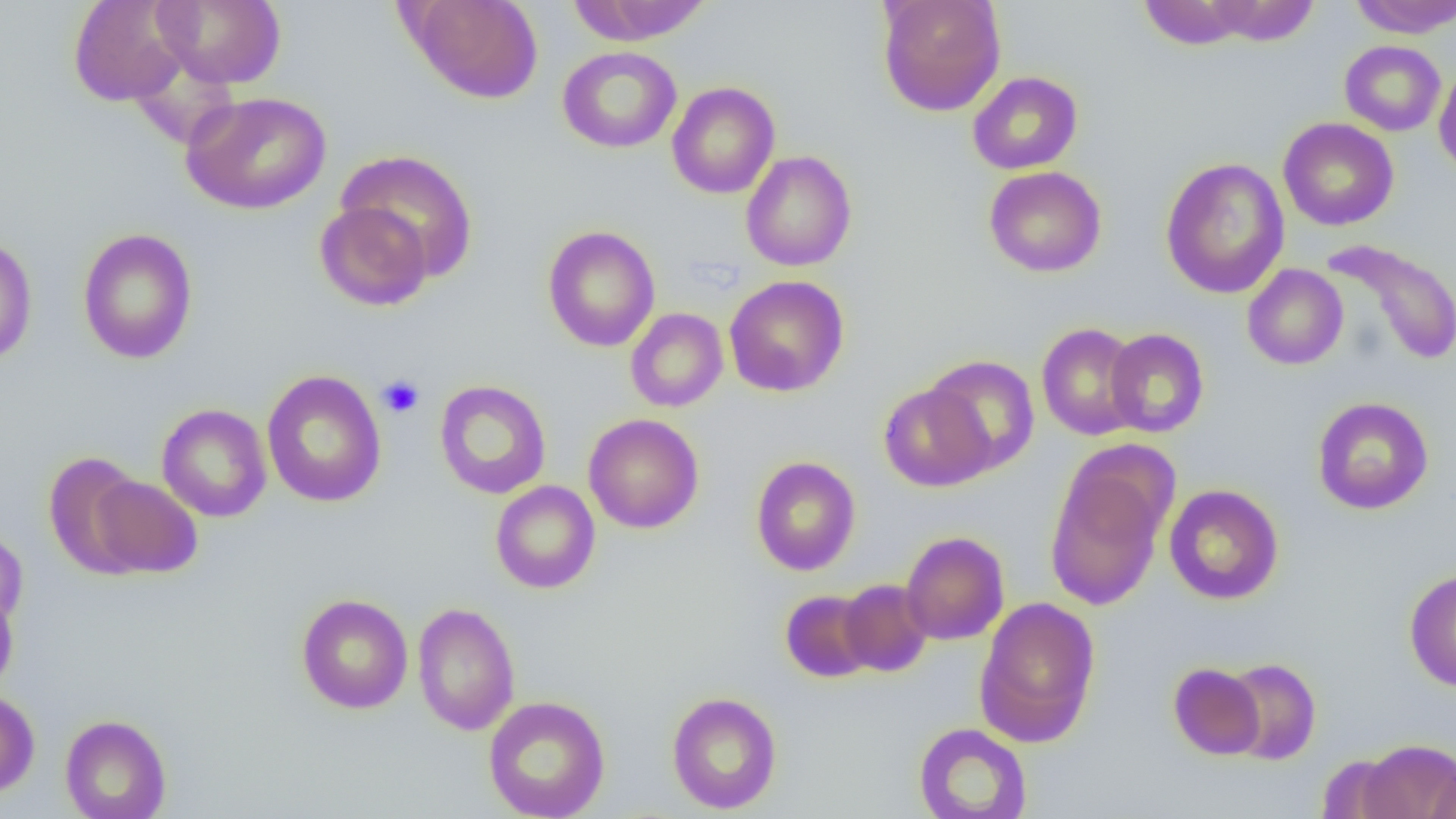
Summary:
  - Coordinate format: approximate bounding boxes as [x1, y1, x2, y2] in pixels
  - Uninfected red blood cell locations: [68, 0, 191, 107], [152, 0, 286, 89], [406, 0, 542, 104], [876, 0, 1007, 116], [1347, 0, 1456, 38], [567, 1, 714, 45], [1138, 1, 1255, 50], [1203, 1, 1320, 46], [1339, 40, 1447, 136], [557, 46, 682, 153], [1434, 64, 1456, 179], [967, 71, 1083, 175], [666, 82, 780, 199], [181, 91, 332, 215], [1278, 117, 1399, 230], [335, 149, 478, 280], [740, 150, 857, 272], [1160, 157, 1289, 299], [984, 166, 1107, 277], [315, 201, 433, 311], [542, 225, 661, 352], [77, 227, 198, 364], [0, 234, 37, 366], [1322, 238, 1456, 367], [1242, 264, 1348, 370], [724, 275, 850, 397], [625, 308, 728, 412], [1036, 322, 1145, 441], [1104, 328, 1210, 437], [922, 355, 1040, 475], [260, 369, 387, 508], [434, 379, 551, 499], [879, 383, 993, 491], [1312, 396, 1434, 515], [156, 404, 272, 523], [584, 413, 704, 534], [42, 452, 149, 577], [750, 456, 861, 576], [1044, 466, 1167, 611], [86, 474, 203, 579], [490, 481, 601, 593], [1163, 484, 1284, 605], [0, 527, 28, 630], [900, 531, 1010, 645], [1404, 568, 1456, 692], [839, 579, 934, 677], [0, 587, 19, 696], [780, 590, 877, 683], [296, 593, 413, 714], [974, 596, 1101, 747], [412, 603, 520, 735], [1223, 658, 1321, 765], [1168, 663, 1265, 760], [0, 689, 40, 799], [666, 691, 782, 814], [483, 695, 610, 819], [60, 714, 172, 819], [913, 723, 1032, 819], [1357, 739, 1455, 819], [1315, 755, 1408, 818], [1428, 759, 1456, 819]
  - Platelet locations: [377, 375, 425, 418]
  - Slide-level diagnosis: no evidence of blood parasites
  - Image size: 1456×819 pixels
  - Magnification: 1000x
  - Preparation: thin blood smear
  - Field of view: single
  - Modality: light microscopy